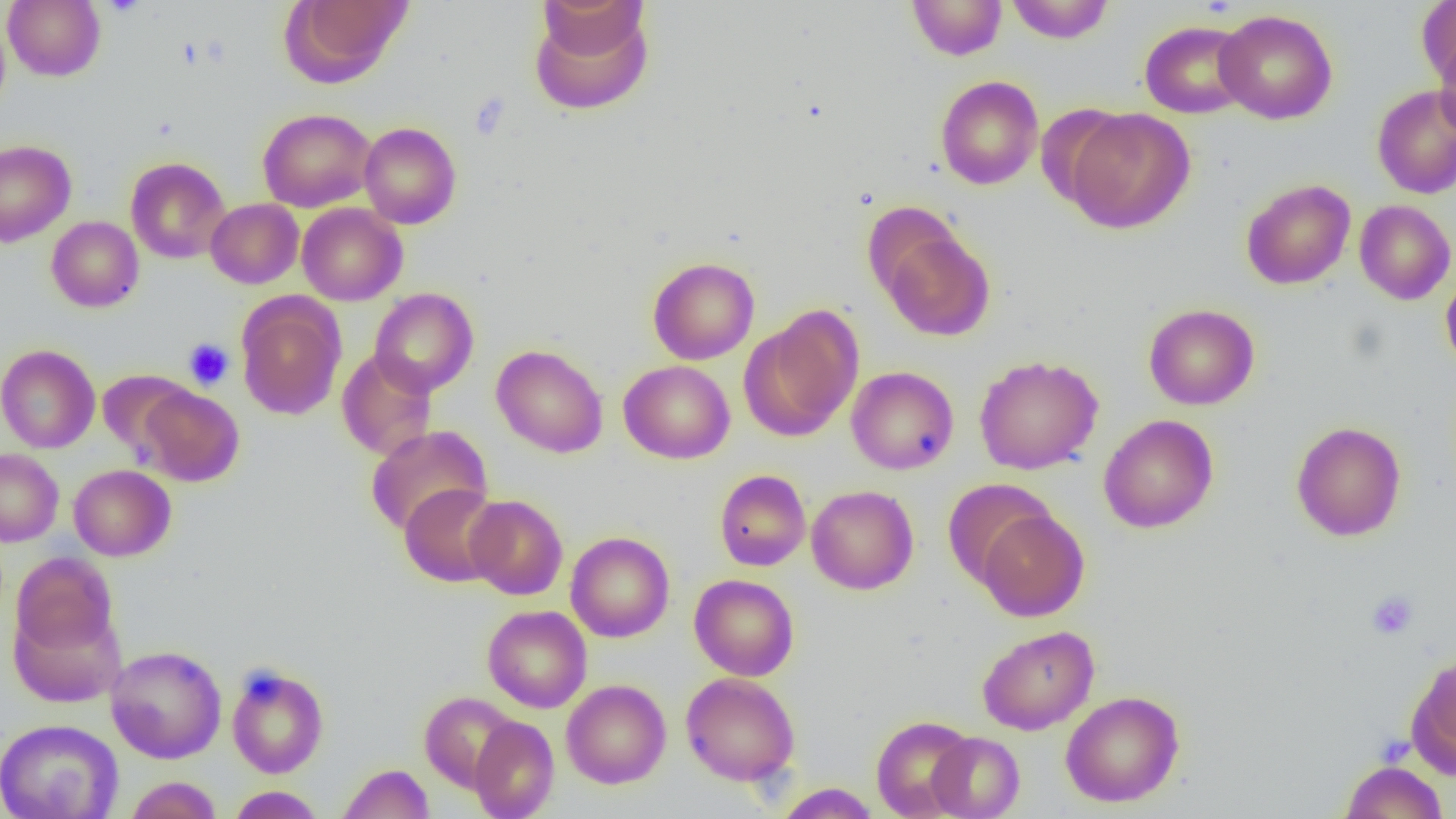

{
  "slide_level_diagnosis": "negative for blood parasites",
  "modality": "optical microscopy",
  "uninfected_red_blood_cell_locations": "approximate bounding boxes as (x1,y1)-(x2,y2) corner pairs in pixels: (3,0)-(105,82), (284,0)-(414,85), (537,0)-(649,58), (907,0)-(1007,60), (1006,0)-(1114,43), (1417,1)-(1456,95), (529,4)-(654,116), (1214,9)-(1338,125), (0,11)-(11,118), (1139,20)-(1252,118), (1434,33)-(1456,142), (935,75)-(1044,190), (1371,84)-(1456,199), (258,108)-(377,212), (1062,108)-(1196,233), (359,121)-(462,229), (0,140)-(76,246), (125,157)-(231,264), (1241,179)-(1356,290), (205,198)-(303,289), (1354,200)-(1455,304), (297,203)-(408,305), (46,216)-(144,312), (879,226)-(994,342), (647,257)-(760,364), (1441,272)-(1456,375), (369,287)-(479,397), (237,295)-(345,420), (1143,303)-(1259,410), (741,309)-(863,440), (0,344)-(100,453), (491,344)-(609,458), (337,349)-(438,461), (974,355)-(1103,475), (618,360)-(735,464), (846,366)-(959,474), (96,369)-(195,460), (136,386)-(244,486), (1099,414)-(1219,533), (1291,421)-(1406,542), (365,425)-(492,536), (0,448)-(63,547), (69,464)-(176,561), (714,469)-(811,571), (944,479)-(1058,587), (399,484)-(505,587), (806,485)-(919,595), (464,494)-(568,600), (974,507)-(1089,621), (565,531)-(675,643), (11,552)-(119,659), (689,574)-(799,681), (482,605)-(593,713), (977,625)-(1099,735), (105,645)-(227,763), (1408,652)-(1456,776), (226,663)-(329,778), (680,672)-(800,786), (561,679)-(671,788), (1060,690)-(1185,807), (420,692)-(520,792), (871,715)-(977,818), (469,716)-(559,819), (1,718)-(122,819), (927,732)-(1024,818), (1340,760)-(1448,819), (338,763)-(433,819), (124,776)-(222,819), (775,783)-(880,818), (226,786)-(325,818)",
  "preparation": "thin blood smear",
  "field_of_view": "one of a larger specimen",
  "image_size": "1456×819 pixels",
  "magnification": "1000x",
  "platelet_locations": "approximate bounding boxes as (x1,y1)-(x2,y2) corner pairs in pixels: (101,0)-(147,17), (183,338)-(234,389), (1366,590)-(1419,640)"
}